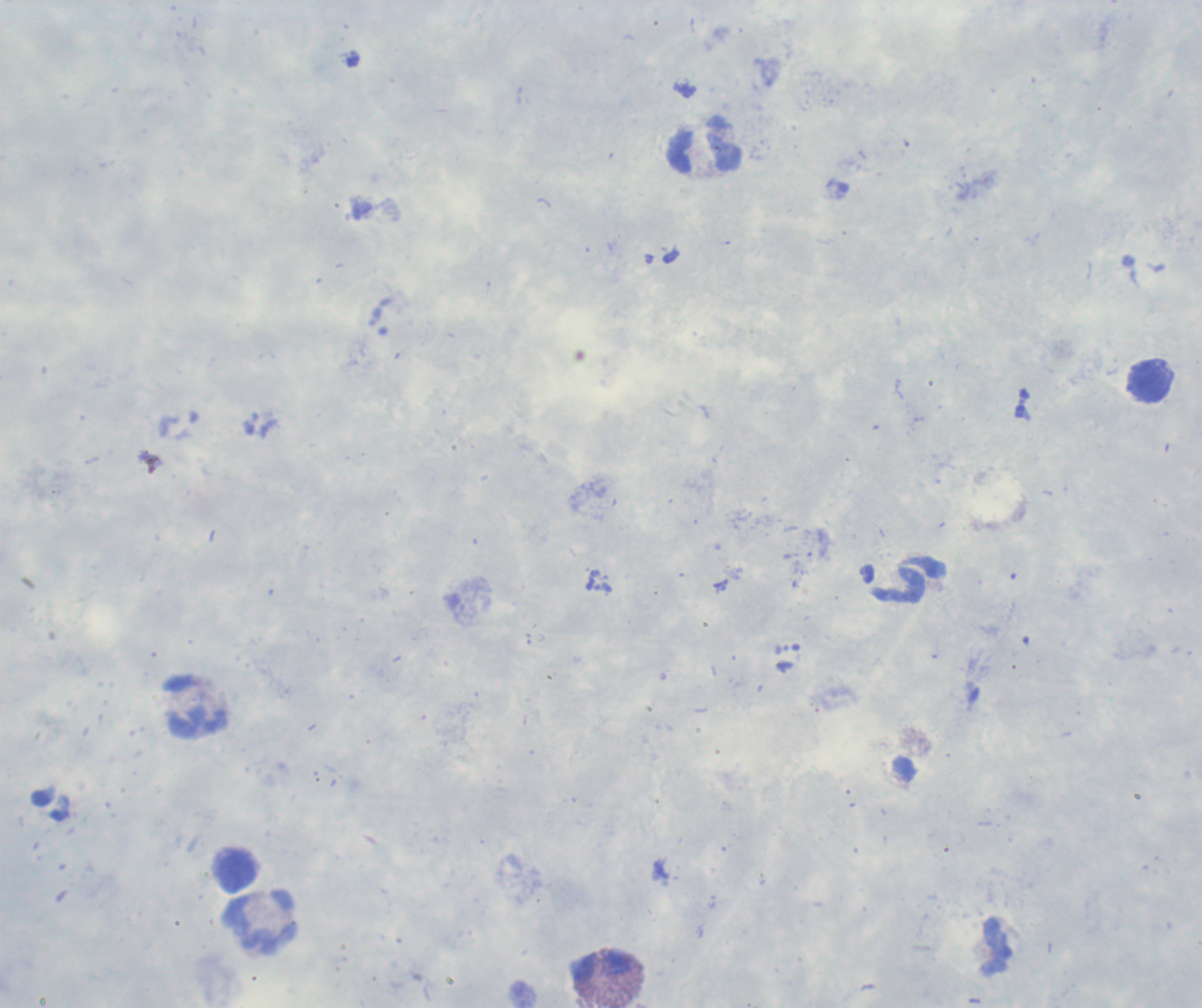
Approximate centers as (x, y) in pixels. Leukocyte locations: (705, 150), (1150, 383), (910, 580), (197, 706), (235, 871), (261, 921), (996, 946), (603, 969). Result: no Plasmodium parasites detected. Image is 1202×1008 pixels. Romanowsky stain. Background quality: poor. Thick blood film. Captured at 100x magnification. Single field of view. Coloration quality: good. Previously used in a real diagnosis.